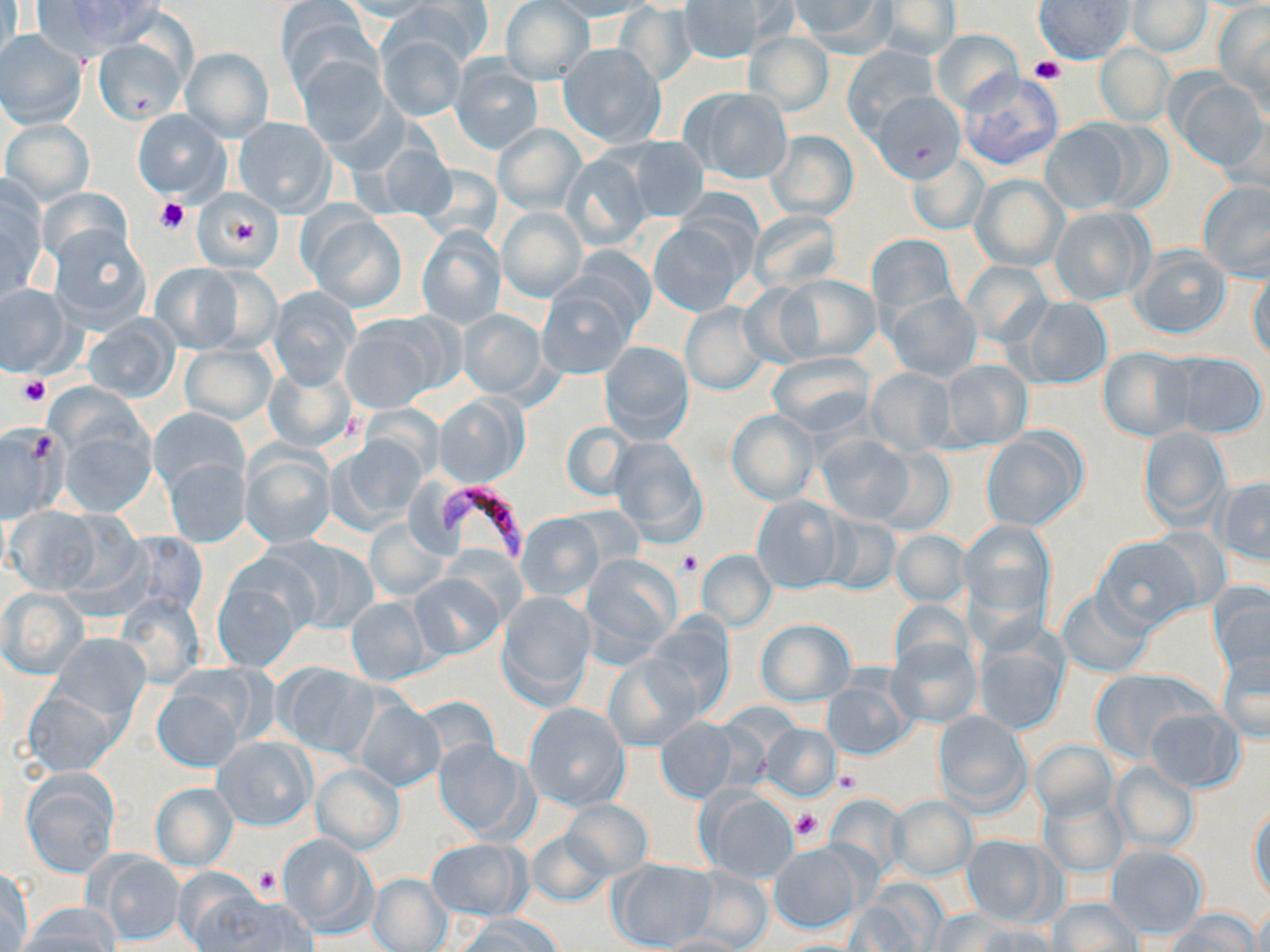
slide-level diagnosis = Plasmodium falciparum
preparation = thin blood film
uninfected red blood cell locations = approximate bounding boxes as [x1, y1, x2, y2] in pixels: [1, 0, 22, 74], [36, 0, 165, 52], [335, 0, 444, 21], [392, 0, 493, 67], [543, 0, 656, 21], [677, 0, 783, 66], [1034, 0, 1133, 64], [277, 1, 375, 94], [501, 1, 594, 86], [786, 1, 895, 55], [874, 1, 960, 62], [1126, 1, 1212, 58], [613, 3, 699, 87], [1215, 3, 1270, 107], [930, 28, 1022, 114], [0, 31, 88, 128], [375, 32, 465, 122], [744, 32, 834, 116], [93, 38, 186, 122], [558, 42, 666, 148], [841, 44, 939, 135], [1094, 44, 1173, 125], [181, 47, 273, 140], [294, 54, 390, 152], [450, 57, 543, 154], [858, 62, 957, 178], [959, 72, 1064, 172], [1172, 75, 1269, 170], [682, 87, 793, 186], [1218, 106, 1270, 194], [132, 109, 230, 202], [233, 117, 336, 217], [4, 119, 94, 203], [1037, 121, 1134, 215], [1092, 121, 1173, 213], [494, 124, 585, 214], [765, 129, 858, 221], [366, 135, 459, 223], [615, 135, 711, 220], [561, 151, 656, 251], [907, 151, 990, 237], [970, 175, 1068, 270], [0, 177, 47, 303], [1199, 181, 1270, 279], [193, 188, 284, 275], [498, 207, 587, 303], [1049, 207, 1151, 306], [303, 209, 406, 311], [748, 211, 842, 290], [650, 219, 749, 316], [417, 226, 505, 330], [47, 227, 152, 332], [865, 232, 958, 322], [1131, 245, 1233, 339], [150, 261, 250, 352], [960, 261, 1052, 347], [1249, 269, 1269, 363], [777, 274, 881, 362], [0, 283, 74, 377], [538, 283, 636, 379], [267, 287, 361, 389], [887, 292, 982, 381], [1019, 296, 1112, 391], [680, 302, 769, 395], [458, 309, 548, 399], [80, 314, 182, 404], [342, 314, 451, 411], [600, 340, 694, 442], [179, 342, 277, 427], [1097, 345, 1194, 442], [1168, 351, 1268, 439], [766, 353, 876, 437], [938, 357, 1032, 450], [262, 359, 358, 454], [864, 367, 956, 456], [434, 393, 528, 486], [149, 407, 250, 502], [728, 410, 818, 504], [55, 417, 155, 516], [560, 420, 634, 503], [0, 423, 69, 521], [1138, 424, 1230, 527], [982, 430, 1085, 531], [817, 433, 917, 524], [327, 435, 428, 532], [606, 437, 707, 545], [240, 444, 336, 548], [874, 445, 955, 537], [164, 456, 251, 548], [1215, 476, 1270, 563], [751, 494, 846, 594], [6, 506, 106, 595], [819, 513, 902, 596], [516, 514, 604, 601], [366, 517, 449, 602], [961, 519, 1055, 619], [116, 530, 209, 621], [892, 530, 968, 608], [265, 536, 378, 633], [1093, 536, 1203, 633], [697, 549, 776, 630], [579, 553, 683, 665], [213, 561, 314, 671], [410, 572, 505, 659], [1209, 583, 1270, 679], [2, 588, 87, 678], [1056, 588, 1155, 679], [496, 590, 596, 708], [116, 594, 204, 688], [345, 594, 432, 685], [890, 599, 971, 674], [645, 616, 737, 717], [756, 619, 853, 705], [50, 632, 151, 723], [887, 638, 980, 728], [972, 638, 1068, 734], [1217, 651, 1269, 742], [603, 653, 700, 752], [275, 663, 381, 760], [1090, 668, 1212, 764], [153, 678, 256, 771], [823, 680, 910, 759], [22, 687, 122, 776], [354, 699, 445, 792], [523, 701, 629, 809], [1146, 707, 1243, 791], [932, 710, 1031, 813], [655, 717, 738, 803], [762, 723, 841, 799], [212, 735, 315, 830], [433, 739, 534, 841], [1029, 739, 1118, 821], [1111, 761, 1199, 853], [311, 763, 404, 854], [20, 768, 120, 876], [151, 782, 239, 871], [699, 789, 800, 883], [1038, 789, 1129, 879], [888, 796, 976, 879], [558, 799, 654, 882], [1249, 805, 1269, 904], [526, 827, 616, 908], [276, 833, 375, 935], [960, 833, 1055, 927], [427, 837, 529, 921], [768, 842, 864, 933], [1107, 845, 1208, 939], [90, 852, 186, 946], [607, 859, 717, 951], [1, 867, 35, 950], [685, 867, 774, 949], [367, 872, 454, 952], [179, 880, 304, 950], [1049, 897, 1142, 951], [17, 903, 121, 952], [929, 909, 1019, 952], [1166, 910, 1258, 952], [456, 915, 560, 952], [649, 935, 751, 952]
platelet locations = approximate bounding boxes as [x1, y1, x2, y2] in pixels: [1029, 57, 1065, 83], [154, 197, 190, 235], [230, 218, 266, 250], [17, 376, 51, 406], [678, 552, 703, 575], [833, 768, 860, 793], [789, 808, 824, 843], [255, 868, 280, 896]
stain = May-Grünwald-Giemsa
modality = light microscopy
Plasmodium falciparum-infected red blood cell locations = approximate bounding boxes as [x1, y1, x2, y2] in pixels: [435, 484, 532, 563]
field of view = single
image size = 1270×952 pixels
magnification = 1000x